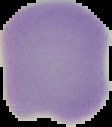
Image is 112×127 pixels. Malaria status: uninfected. From a thin blood smear. The area outside the segmented cell region is set to black.